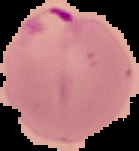

Summary:
  - Image type: segmented cell region on a black background
  - Result: malaria parasites detected
  - Preparation: thin blood film
  - Image size: 139×151 pixels